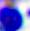

400x magnification. A white blood cell is shown. Micrograph.